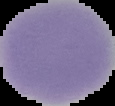 Image is 115×106 pixels. Malaria status: uninfected. From a thin blood film. Segmented cell region on a black background.